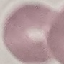

result = no malaria parasites detected
preparation = thin smear
stain = Giemsa
capture = smartphone through the microscope eyepiece
image type = automatically extracted cell patch, resized to 64 × 64 pixels